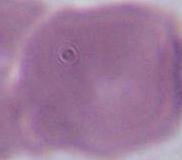
Summary:
  - Magnification: 1000x
  - Modality: micrograph
  - Identification: erythrocyte